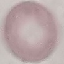
Summary:
  - Result: no malaria parasites seen
  - Preparation: thin smear
  - Stain: Giemsa
  - Capture: smartphone camera at the microscope eyepiece
  - Image type: cell patch, automatically extracted from a larger field of view and resized to 64 × 64 pixels